Point out each malaria parasite.
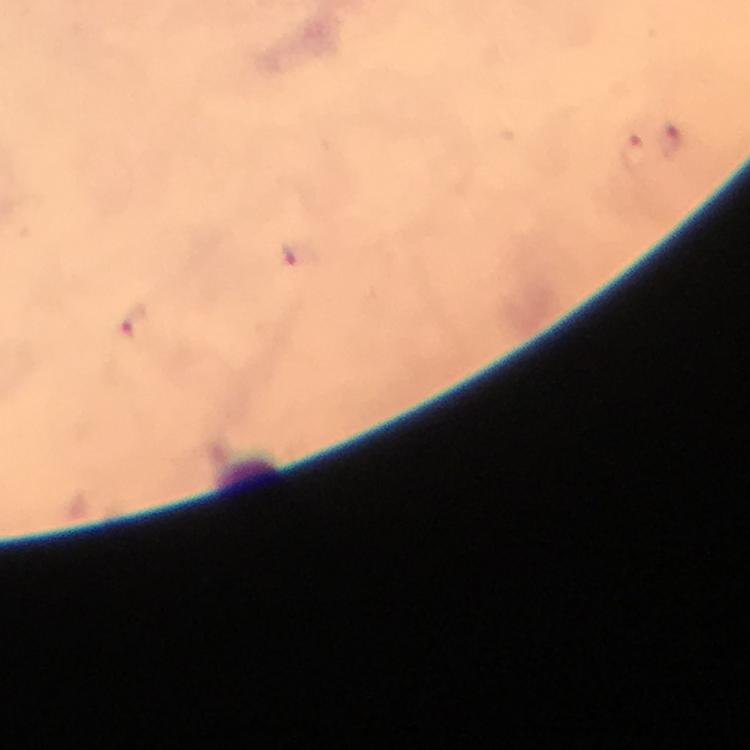
Approximate centers as {x, y} in pixels.
Malaria parasites: {670, 144}, {631, 152}, {297, 257}, {132, 320}.

Summary:
  - Context: from a malaria diagnostic workup
  - Preparation: thick blood smear
  - Image size: 750×750 pixels
  - Immersion oil: used
  - Cropped from: a single field of view
  - Stain: Giemsa
  - Magnification: 100x
  - Capture: smartphone camera through the microscope